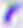

modality: micrograph
magnification: 400x
identification: Toxoplasma gondii